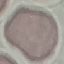
Malaria status: uninfected. Giemsa-stained preparation. Automatically extracted cell patch, resized to 64 × 64 pixels. Photographed with a smartphone camera at the microscope eyepiece. Thin blood film.